Assess for malaria.
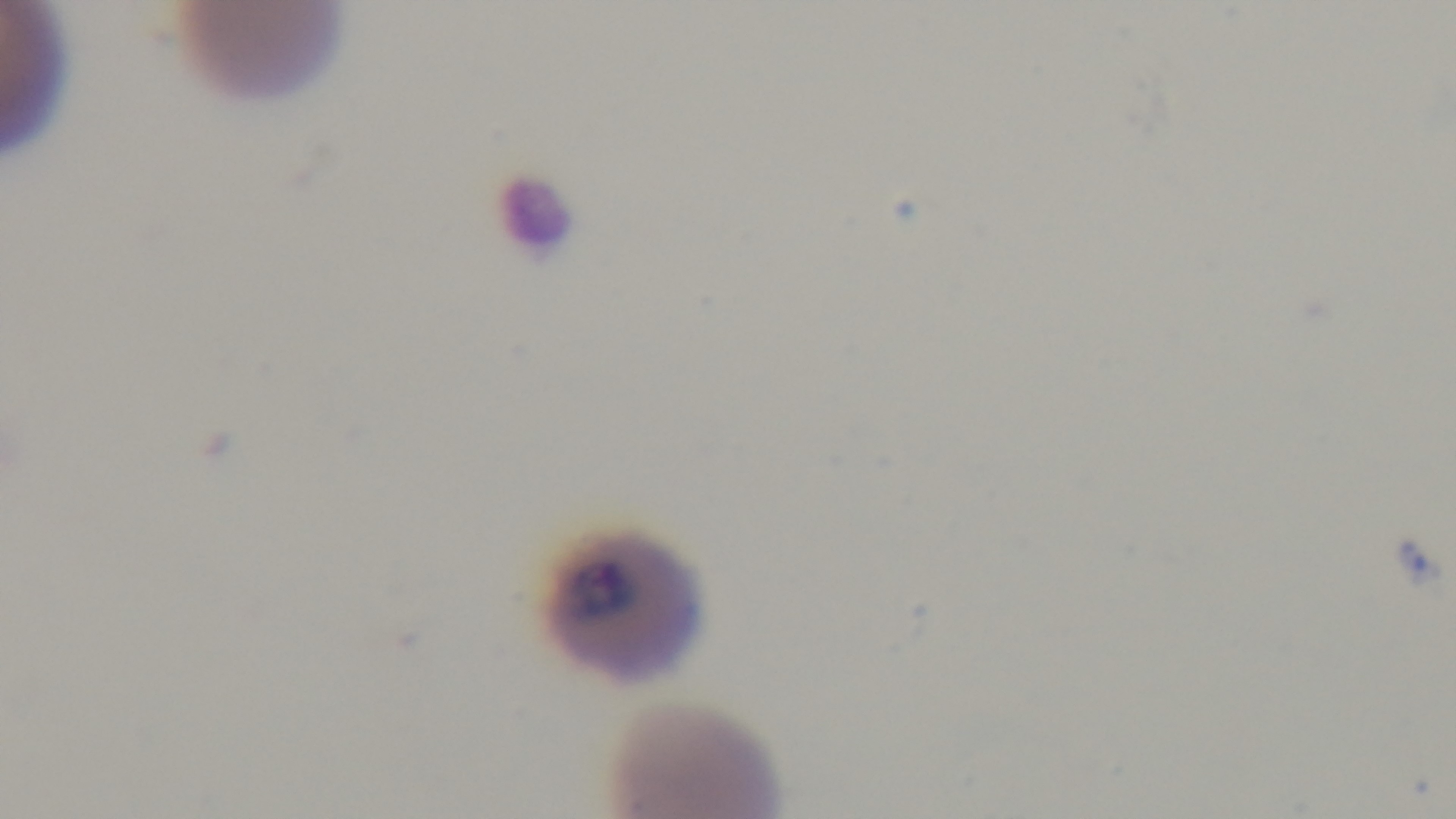
It is infected.

field of view = one from the slide
objective = 100x oil immersion
modality = light microscopy
capture = mounted 4K digital camera
stain = Giemsa
preparation = thin blood film